Name the parasite shown.
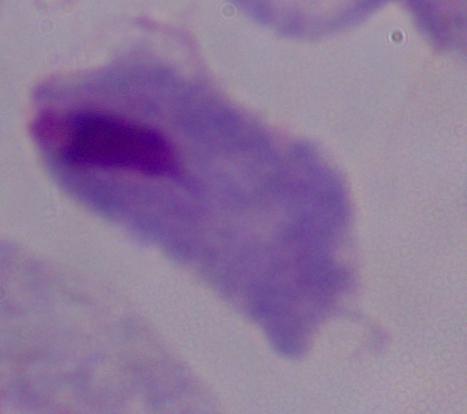
This is a trichomonad.

1000x magnification. Photomicrograph.